Classify the preparation.
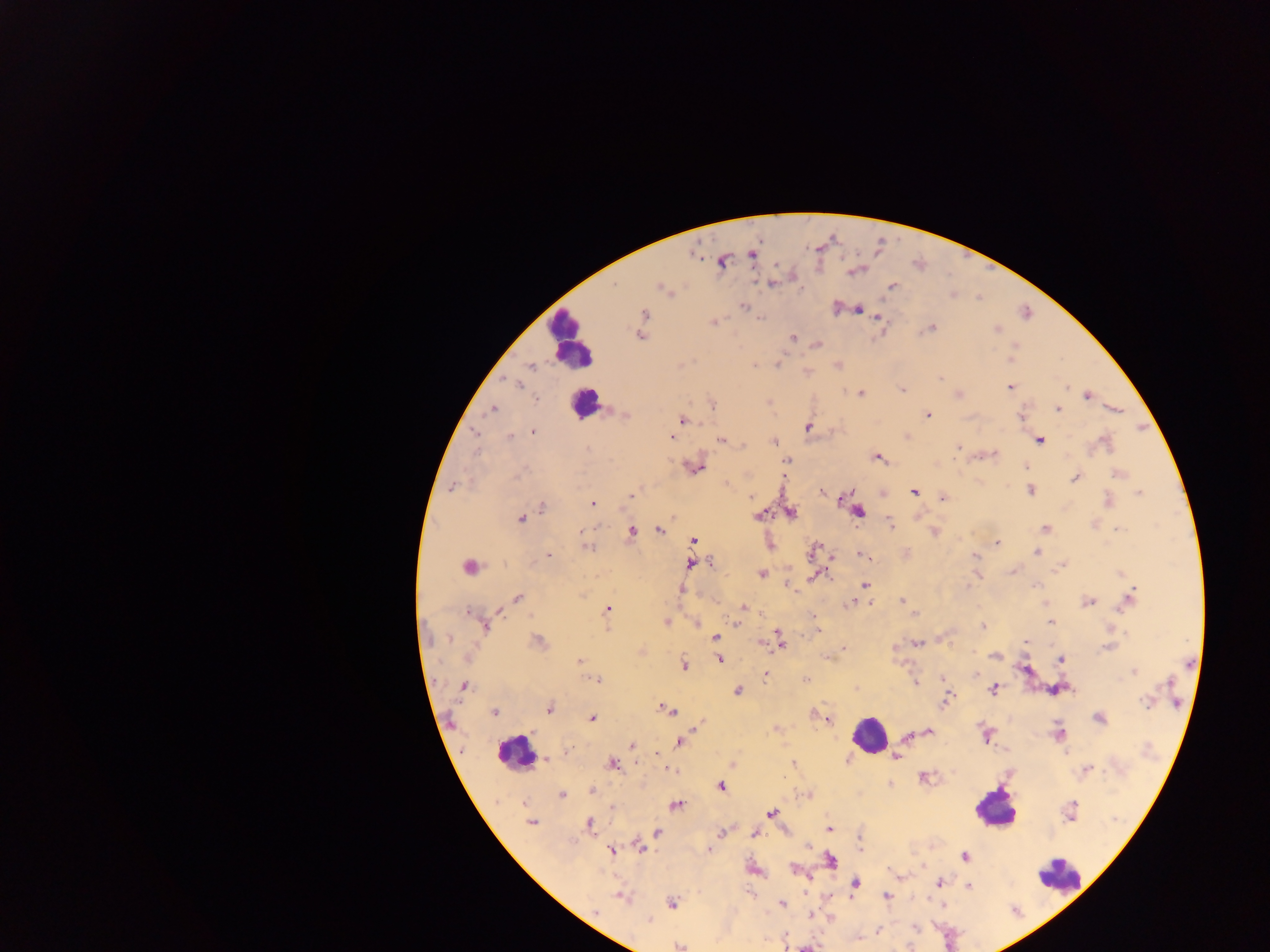
This is a thick smear.

Approximate centers as {x, y} in pixels. Leukocyte locations: {570, 338}, {584, 404}, {868, 735}, {513, 754}, {994, 808}, {1058, 877}. Malaria parasite locations: {752, 254}, {721, 261}, {614, 285}, {772, 285}, {893, 286}, {661, 287}, {742, 306}, {858, 310}, {644, 315}, {878, 316}, {761, 318}, {713, 322}, {932, 327}, {996, 330}, {639, 336}, {793, 338}, {817, 344}, {1011, 357}, {532, 366}, {754, 366}, {940, 378}, {518, 385}, {1010, 387}, {1066, 387}, {903, 390}, {860, 394}, {958, 395}, {1087, 396}, {537, 399}, {712, 406}, {493, 410}, {1058, 410}, {624, 414}, {928, 415}, {1021, 417}, {682, 420}, {807, 427}, {533, 432}, {475, 433}, {509, 436}, {672, 438}, {721, 441}, {1040, 441}, {774, 442}, {1105, 442}, {958, 447}, {587, 449}, {993, 454}, {877, 458}, {787, 460}, {1027, 466}, {698, 468}, {522, 472}, {1118, 474}, {1076, 478}, {453, 487}, {1030, 490}, {821, 492}, {850, 492}, {914, 492}, {1139, 493}, {631, 496}, {751, 497}, {943, 497}, {1109, 501}, {592, 504}, {542, 507}, {858, 512}, {791, 513}, {759, 515}, {520, 518}, {890, 523}, {1045, 528}, {1118, 529}, {660, 530}, {631, 532}, {934, 532}, {695, 540}, {997, 543}, {587, 547}, {814, 549}, {1035, 552}, {862, 555}, {975, 555}, {549, 556}, {690, 563}, {711, 563}, {1062, 566}, {469, 567}, {1011, 571}, {762, 573}, {815, 574}, {865, 584}, {787, 585}, {1036, 585}, {680, 590}, {582, 595}, {1131, 596}, {517, 598}, {901, 600}, {1088, 602}, {851, 603}, {744, 608}, {608, 609}, {469, 612}, {915, 614}, {813, 617}, {667, 622}, {1051, 622}, {697, 623}, {736, 623}, {485, 626}, {983, 626}, {777, 635}, {715, 637}, {449, 639}, {538, 641}, {779, 641}, {1026, 642}, {762, 643}, {917, 643}, {844, 648}, {1108, 648}, {995, 656}, {467, 657}, {827, 657}, {719, 660}, {1061, 660}, {580, 661}, {684, 665}, {1024, 670}, {1133, 671}, {765, 676}, {806, 679}, {943, 679}, {598, 681}, {1170, 682}, {916, 683}, {464, 686}, {993, 688}, {737, 691}, {949, 694}, {946, 699}, {1146, 702}, {549, 709}, {667, 710}, {494, 713}, {592, 718}, {1098, 718}, {828, 720}, {699, 723}, {928, 732}, {1059, 734}, {985, 736}, {907, 737}, {680, 742}, {632, 745}, {569, 751}, {896, 757}, {547, 759}, {613, 763}, {793, 763}, {671, 770}, {1086, 770}, {924, 778}, {720, 787}, {592, 791}, {562, 794}, {677, 805}, {612, 809}, {1071, 811}, {771, 813}, {531, 823}, {589, 824}, {828, 828}, {657, 832}, {721, 833}, {754, 834}, {859, 843}, {640, 847}, {709, 849}, {612, 851}, {965, 856}, {831, 861}, {794, 869}, {939, 882}, {856, 884}, {968, 887}, {887, 895}, {621, 896}, {672, 903}, {781, 904}, {595, 911}, {648, 920}, {916, 928}, {878, 931}, {679, 946}, {806, 948}. One field of view. Sample from Ghana. Image is 1270×952 pixels. Mobile-phone photograph taken through the microscope.